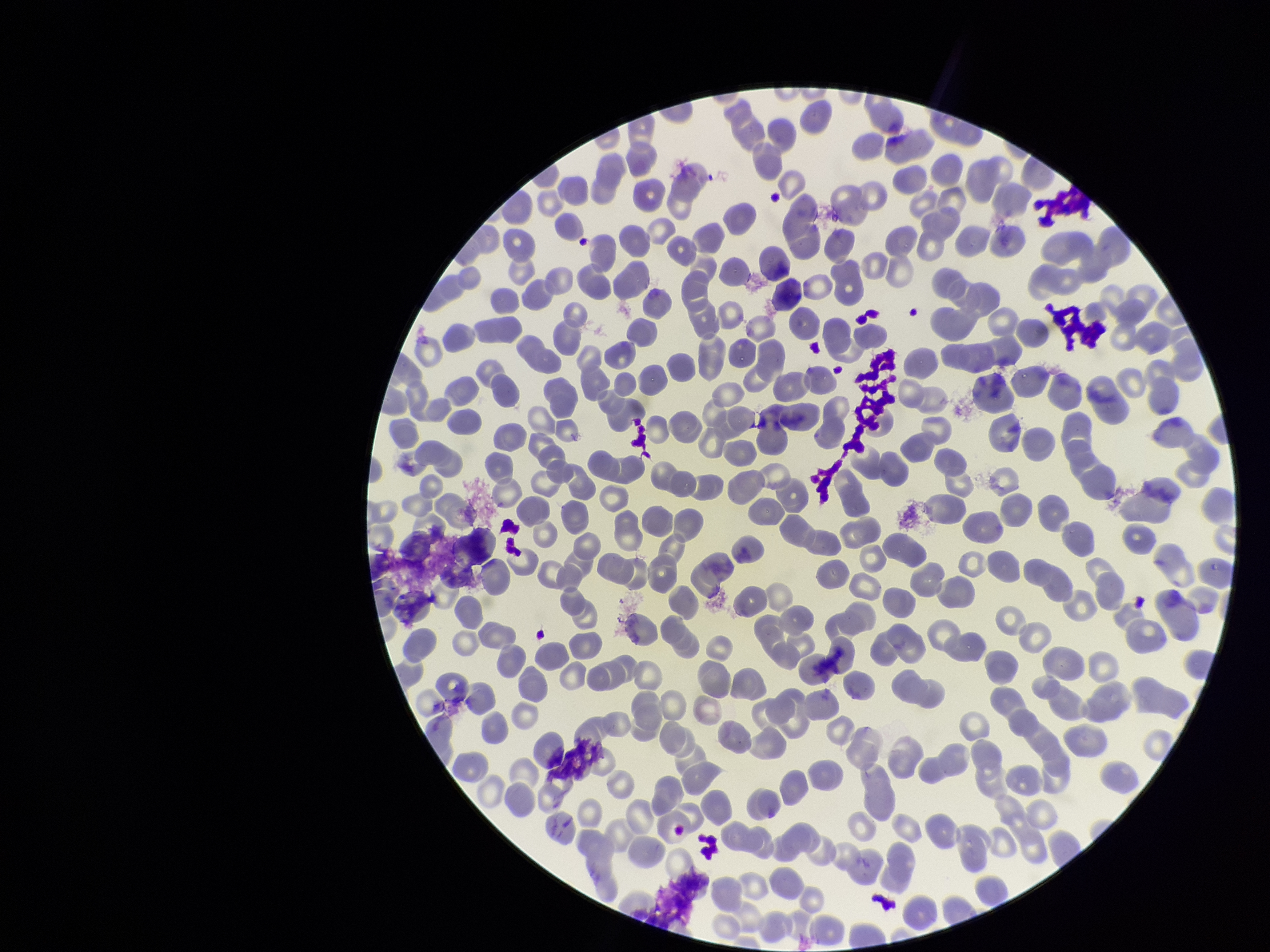

Giemsa stain. Parasitized red blood cell count: 0. Parasitized red blood cells: none detected. Patient malaria status: negative. Smartphone photograph taken through the eyepiece of a microscope. Red blood cell count: 265. Single field of view. Preparation: thin smear. Image is 1270×952 pixels.